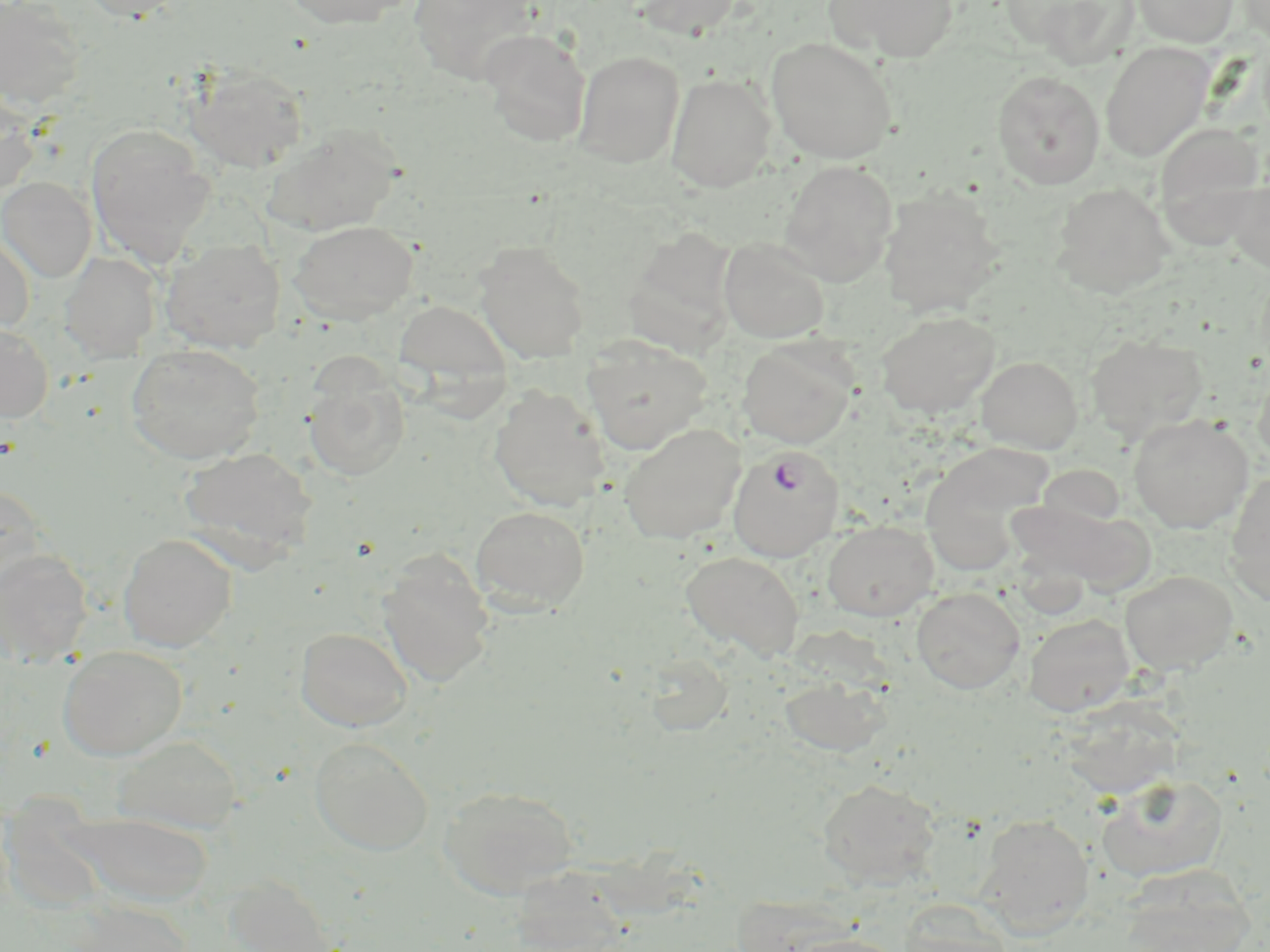 Approximate bounding boxes as (x1,y1)-(x2,y2) corner pairs in pixels. Uninfected red blood cell locations: (0,0)-(88,110), (78,0)-(189,22), (280,0)-(415,29), (410,0)-(540,85), (633,0)-(742,39), (824,0)-(958,64), (1132,0)-(1238,47), (1238,0)-(1270,45), (1021,1)-(1141,68), (479,28)-(591,147), (766,37)-(898,164), (1100,42)-(1213,162), (573,49)-(685,168), (184,65)-(309,174), (992,71)-(1105,190), (666,73)-(775,192), (0,95)-(41,200), (85,123)-(215,266), (1155,123)-(1265,240), (264,124)-(402,237), (779,160)-(898,286), (0,176)-(97,282), (1227,177)-(1270,272), (1052,182)-(1175,298), (880,187)-(1005,317), (289,220)-(419,325), (626,224)-(749,373), (0,227)-(35,336), (160,238)-(286,353), (718,238)-(830,343), (474,242)-(590,363), (60,251)-(160,361), (394,298)-(512,394), (876,310)-(1001,418), (0,322)-(53,423), (1086,333)-(1208,441), (581,337)-(712,455), (737,338)-(857,449), (125,344)-(265,464), (976,356)-(1083,453), (1253,366)-(1270,471), (303,372)-(410,482), (489,384)-(610,511), (1128,413)-(1254,532), (618,423)-(746,544), (920,443)-(1055,575), (179,447)-(318,562), (1224,471)-(1270,605), (0,483)-(48,593), (1009,495)-(1148,590), (471,505)-(590,613), (822,520)-(938,621), (117,533)-(237,651), (0,549)-(93,666), (681,550)-(805,660), (376,551)-(495,687), (1120,570)-(1238,676), (911,588)-(1025,693), (1024,614)-(1135,717), (295,627)-(413,732), (57,645)-(188,760), (642,651)-(734,734), (778,673)-(891,760), (1058,695)-(1187,799), (113,735)-(243,833), (309,736)-(434,855), (1097,776)-(1228,882), (817,779)-(941,888), (439,785)-(579,899), (66,811)-(214,907), (976,813)-(1094,937), (518,863)-(630,947), (1119,864)-(1255,952), (224,875)-(340,952), (66,900)-(194,952), (898,900)-(1013,952), (780,933)-(908,952). Plasmodium falciparum-infected red blood cell locations: (728,445)-(845,562). Slide-level diagnosis: Plasmodium falciparum. Thin blood film. Image is 1270×952 pixels. May-Grünwald-Giemsa-stained preparation. Captured at 1000x magnification. Single field of view. Optical microscopy.